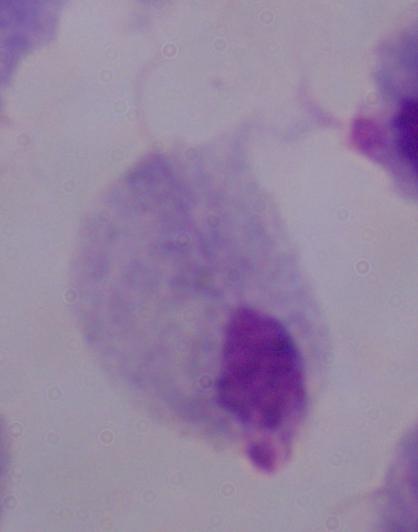

identification = trichomonad
modality = micrograph
magnification = 1000x